Assess this cell for malaria.
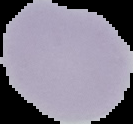
It is uninfected.

Summary:
  - Preparation: thin blood smear
  - Image type: cell region segmented out of the field of view; surrounding area masked to black
  - Image size: 133×124 pixels